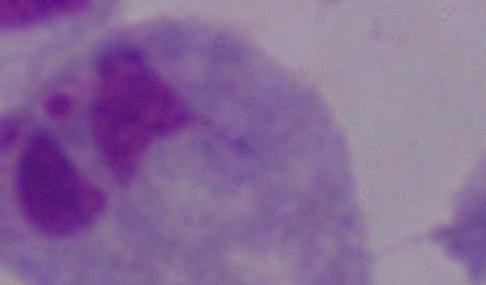
Summary:
  - Magnification: 1000x
  - Modality: photomicrograph
  - Identification: trichomonad